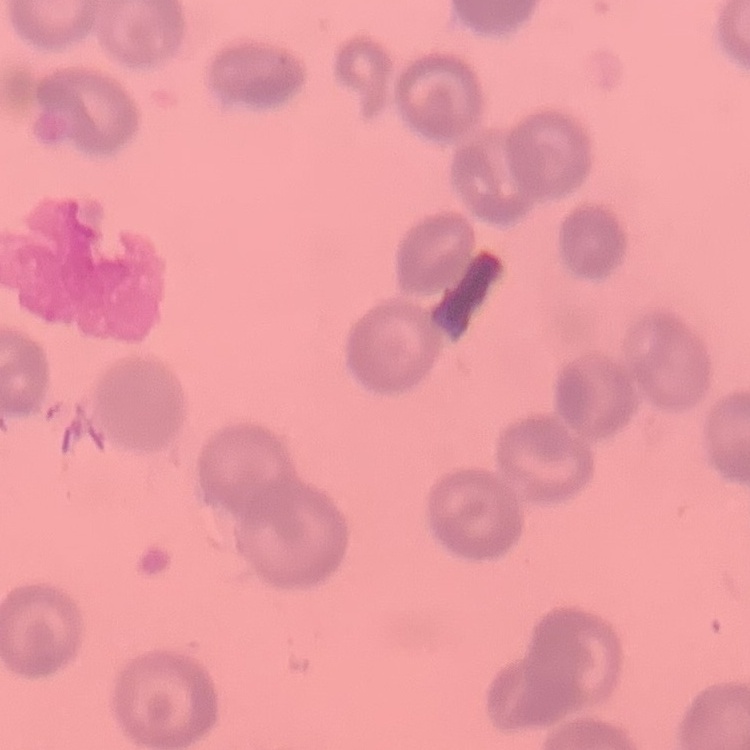 The red blood cells exhibit rouleaux formation. Stained with either Field's or Giemsa. Thin blood film. One tile cut from a larger photomicrograph.